Report the malaria status of this cell.
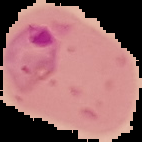

Parasitized.

preparation: thin blood film
image_size: 142×142 pixels
image_type: segmented cell region with the area outside set to black